Give the position of every malaria parasite.
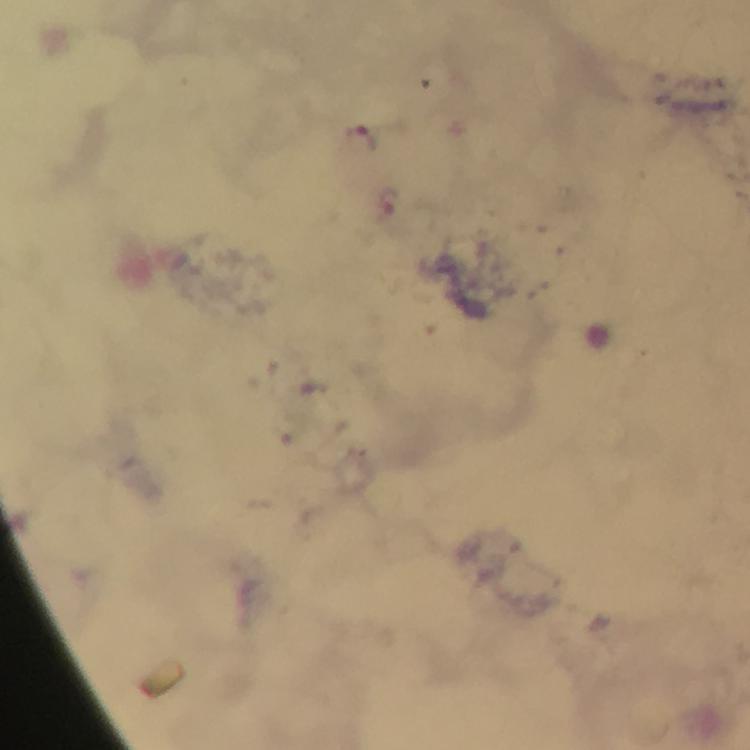

Approximate centers as (x, y) in pixels.
Malaria parasites: (361, 134), (389, 204).

Thick blood smear. From a malaria diagnostic workup. Giemsa-stained preparation. Photographed through the microscope with a smartphone camera. Cropped region of a single field of view. Immersion oil applied. At 100x magnification. Image is 750×750 pixels.